Give the position of every leukocyte visible.
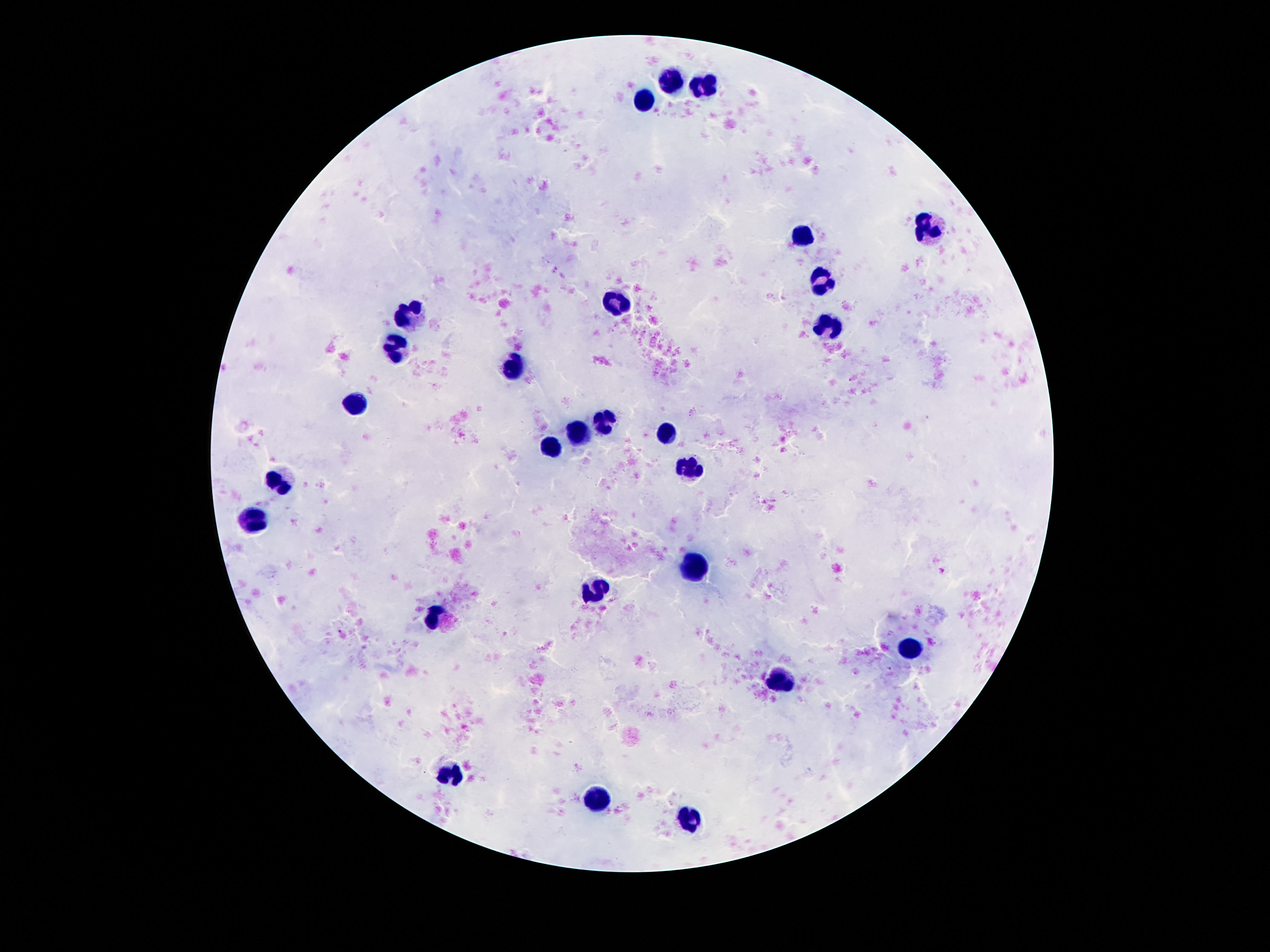
Approximate centers as [x, y] in pixels.
Leukocytes: [672, 80], [704, 88], [645, 99], [932, 229], [808, 235], [823, 280], [613, 301], [409, 315], [827, 328], [395, 349], [514, 366], [357, 403], [603, 419], [580, 431], [662, 436], [550, 448], [689, 467], [283, 480], [252, 522], [693, 564], [594, 590], [435, 617], [913, 651], [781, 682], [449, 771], [596, 800], [691, 822].

Summary:
  - Capture: smartphone camera through the microscope eyepiece
  - Stain: Giemsa
  - Preparation: thick peripheral-blood smear
  - Magnification: 100x
  - Image size: 1270×952 pixels
  - Field of view: one from this slide
  - Patient malaria status: negative